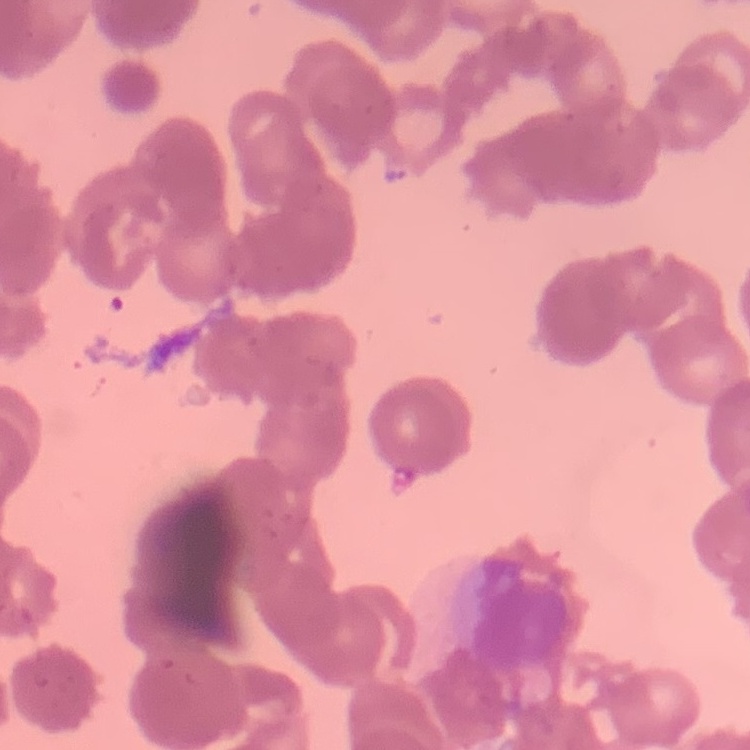
red blood cell morphology = rouleaux formation
stain = Field's or Giemsa
preparation = thin blood smear
image type = square crop of a larger photomicrograph